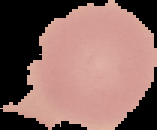

The area outside the segmented cell region is set to black. Result: no malaria parasites seen. From a thin blood film. Image is 157×130 pixels.